Classify this cell by malaria status.
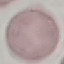

It is uninfected.

image_type: automatically extracted cell patch, resized to 64 × 64 pixels
capture: smartphone through the microscope eyepiece
preparation: thin smear
stain: Giemsa